State which parasite is depicted.
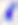

This is Toxoplasma gondii.

Summary:
  - Magnification: 400x
  - Modality: micrograph